Classify this cell by malaria status.
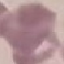

Uninfected.

Cell patch, automatically extracted from a larger field of view and resized to 64 × 64 pixels. Giemsa stain. Thin smear of blood. Acquired by smartphone through the microscope eyepiece.